Assess the morphology of the red blood cells.
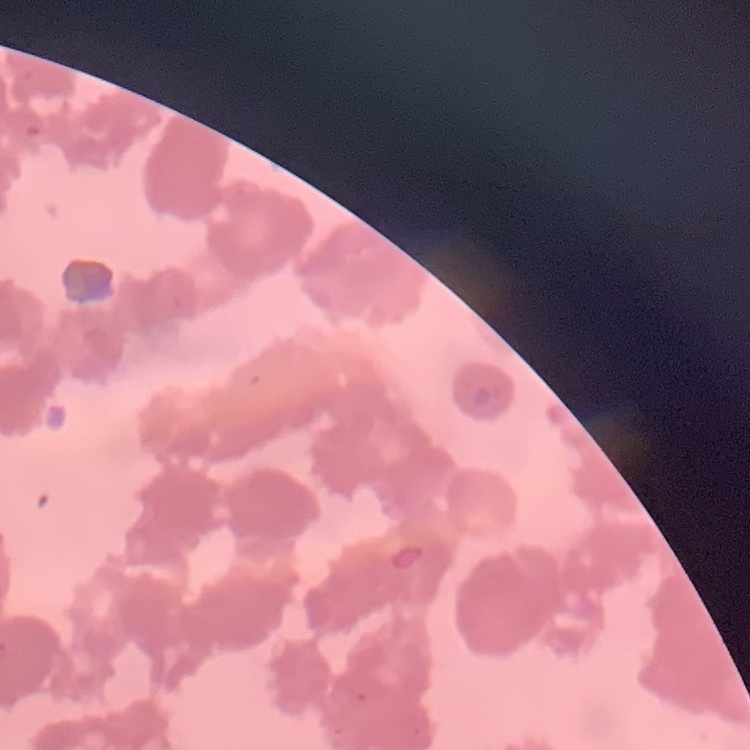

Rouleaux formation.

Thin blood film. Field's or Giemsa stain. Square crop of a larger photomicrograph.